Comment on the morphology of the erythrocytes.
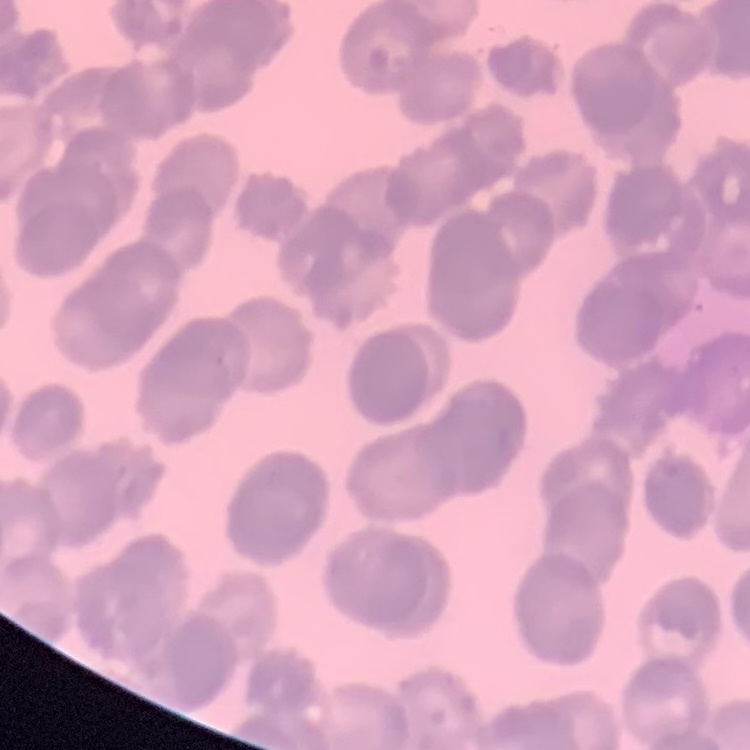

Rouleaux formation.

Summary:
  - Stain: Field's or Giemsa
  - Image type: square crop of a larger photomicrograph
  - Preparation: thin blood film